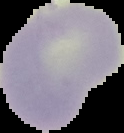

Summary:
  - Preparation: thin blood film
  - Image type: segmented cell region with the area outside set to black
  - Result: no Plasmodium parasites detected
  - Image size: 124×133 pixels